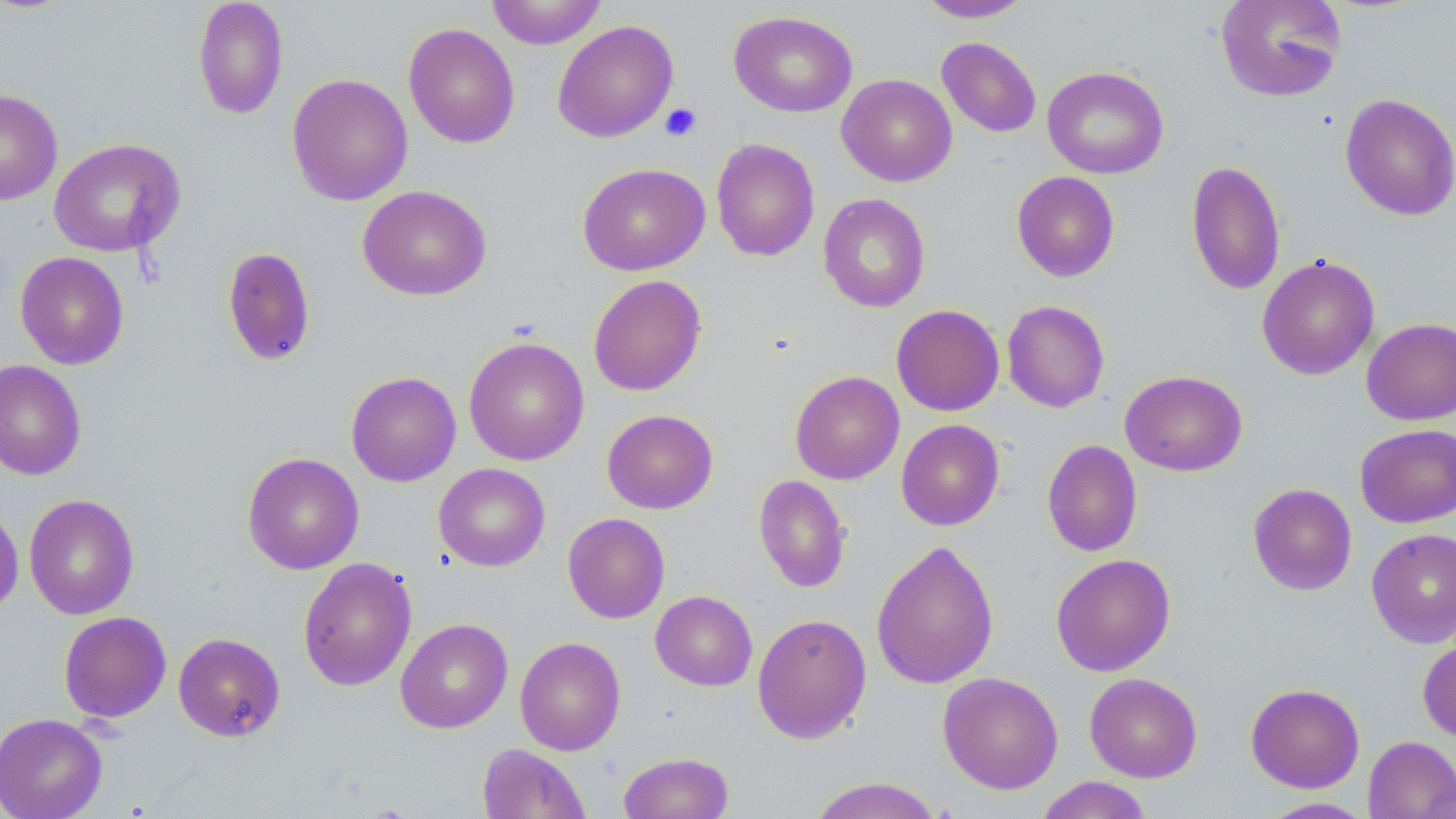
slide-level diagnosis = no evidence of blood parasites
stain = May-Grünwald-Giemsa
modality = optical microscopy
uninfected red blood cell locations = approximate bounding boxes as (x1,y1)-(x2,y2) corner pairs in pixels: (192,0)-(289,119), (486,0)-(607,49), (915,0)-(1033,22), (1214,0)-(1346,103), (728,10)-(858,117), (552,20)-(678,143), (403,23)-(520,148), (936,37)-(1041,137), (1042,65)-(1169,179), (287,73)-(413,206), (837,74)-(957,187), (0,89)-(63,205), (1339,93)-(1456,221), (48,137)-(184,257), (711,138)-(820,262), (1186,159)-(1286,295), (577,162)-(710,276), (1011,171)-(1120,282), (358,185)-(492,301), (818,193)-(930,313), (221,246)-(316,367), (15,251)-(129,369), (1257,254)-(1380,380), (588,274)-(707,396), (1002,300)-(1110,413), (891,304)-(1004,416), (1361,318)-(1456,425), (463,336)-(589,466), (0,359)-(87,481), (790,370)-(905,485), (1120,370)-(1247,476), (345,371)-(462,487), (602,409)-(718,514), (896,419)-(1004,530), (1355,423)-(1456,528), (1042,439)-(1142,557), (242,452)-(364,574), (433,463)-(550,571), (753,474)-(851,593), (1247,483)-(1357,596), (24,493)-(140,620), (0,503)-(24,617), (563,513)-(670,623), (1366,528)-(1456,648), (871,539)-(999,690), (1051,553)-(1176,676), (297,557)-(417,691), (650,590)-(758,691), (58,611)-(171,723), (752,612)-(872,744), (395,617)-(513,734), (173,632)-(286,742), (514,636)-(626,755), (1418,637)-(1456,743), (937,671)-(1063,795), (1084,672)-(1203,782), (1245,683)-(1365,792), (0,712)-(108,819), (1363,735)-(1456,819), (477,743)-(590,819), (618,751)-(734,818), (1036,776)-(1153,819), (806,777)-(945,819), (1258,797)-(1375,818)
preparation = thin blood film
field of view = single
image size = 1456×819 pixels
magnification = 1000x
platelet locations = approximate bounding boxes as (x1,y1)-(x2,y2) corner pairs in pixels: (659,102)-(702,142)